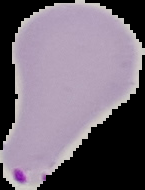

image_type: segmented cell region on a black background
image_size: 145×190 pixels
preparation: thin blood smear
malaria_status: parasitized